Comment on the morphology of the erythrocytes.
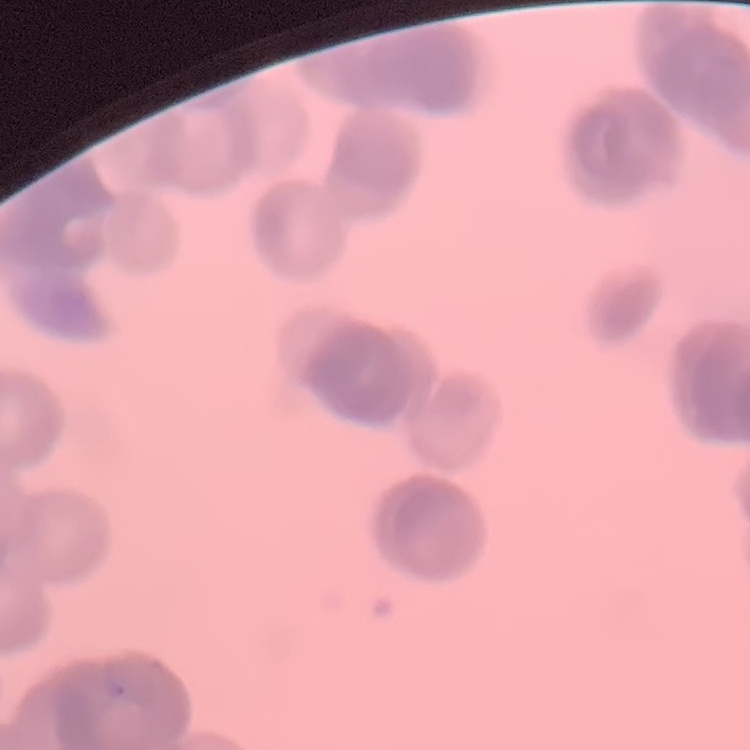

Rouleaux formation.

preparation = thin blood film
stain = Field's or Giemsa
image type = square crop of a larger photomicrograph